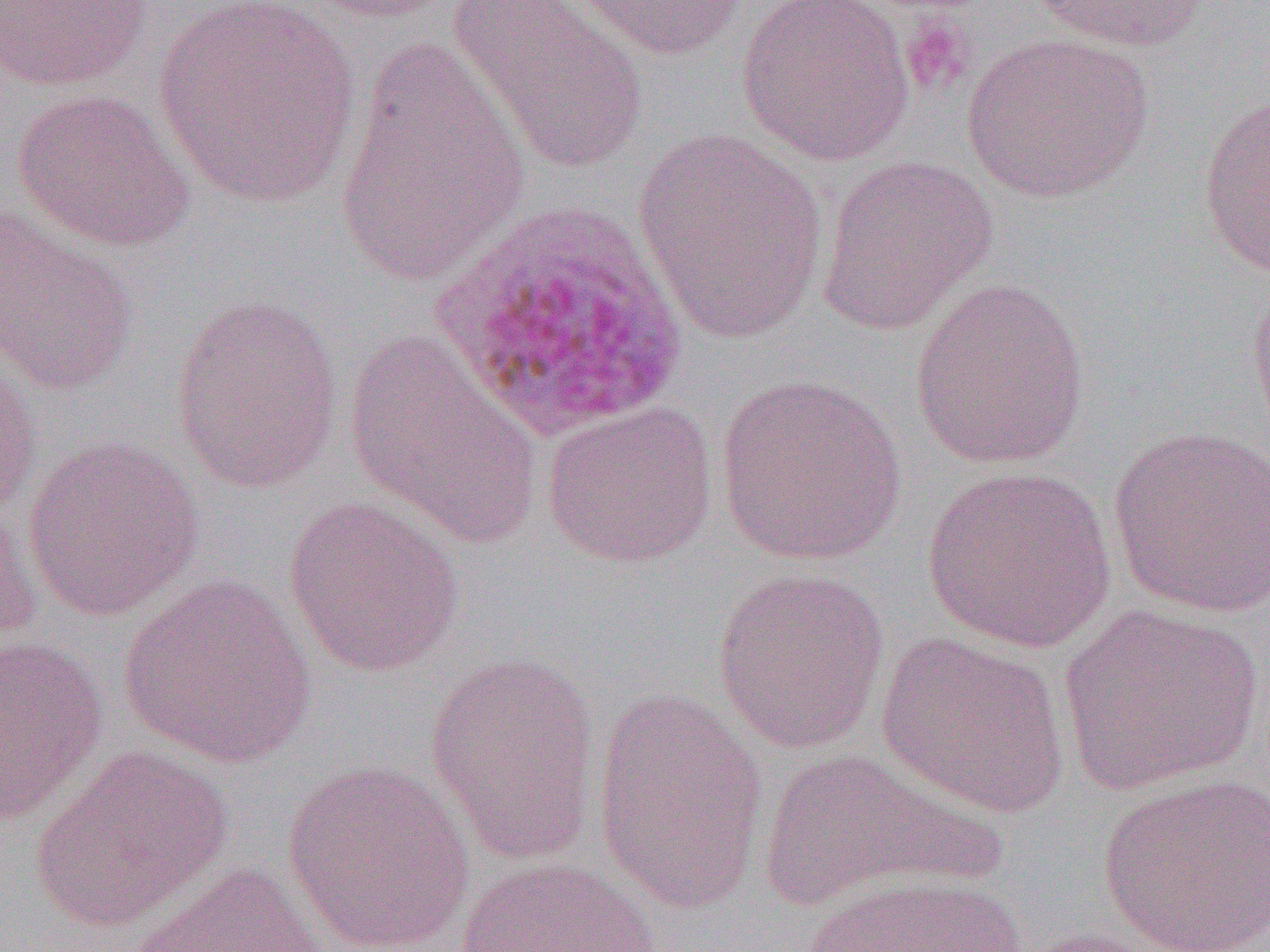
slide_level_diagnosis: Plasmodium ovale
magnification: 1000x
preparation: thin blood smear
platelet_locations: 'approximate bounding boxes as named x1/y1/x2/y2 corners in pixels: (x1=900, y1=14, x2=977, y2=94)'
uninfected_red_blood_cell_locations: 'approximate bounding boxes as named x1/y1/x2/y2 corners in pixels: (x1=1, y1=0, x2=153, y2=91), (x1=294, y1=0, x2=456, y2=23), (x1=447, y1=0, x2=650, y2=176), (x1=565, y1=0, x2=746, y2=62), (x1=735, y1=0, x2=919, y2=167), (x1=1030, y1=0, x2=1218, y2=53), (x1=151, y1=1, x2=365, y2=209), (x1=960, y1=32, x2=1155, y2=204), (x1=336, y1=34, x2=532, y2=291), (x1=11, y1=88, x2=194, y2=252), (x1=1198, y1=94, x2=1270, y2=279), (x1=632, y1=128, x2=831, y2=346), (x1=815, y1=154, x2=998, y2=335), (x1=0, y1=206, x2=141, y2=396), (x1=1247, y1=268, x2=1270, y2=450), (x1=909, y1=277, x2=1091, y2=469), (x1=169, y1=293, x2=343, y2=494), (x1=343, y1=329, x2=545, y2=552), (x1=0, y1=354, x2=42, y2=521), (x1=714, y1=372, x2=909, y2=566), (x1=540, y1=400, x2=718, y2=569), (x1=1106, y1=424, x2=1270, y2=619), (x1=21, y1=436, x2=205, y2=622), (x1=921, y1=465, x2=1117, y2=654), (x1=284, y1=496, x2=465, y2=677), (x1=0, y1=499, x2=41, y2=653), (x1=712, y1=566, x2=891, y2=754), (x1=117, y1=574, x2=318, y2=769), (x1=1057, y1=603, x2=1265, y2=795), (x1=875, y1=630, x2=1072, y2=820), (x1=1, y1=636, x2=109, y2=828), (x1=424, y1=652, x2=602, y2=865), (x1=590, y1=691, x2=769, y2=913), (x1=29, y1=746, x2=233, y2=932), (x1=757, y1=746, x2=998, y2=909), (x1=281, y1=759, x2=476, y2=952), (x1=1098, y1=773, x2=1270, y2=952), (x1=454, y1=857, x2=664, y2=952), (x1=129, y1=861, x2=337, y2=952), (x1=797, y1=873, x2=1032, y2=952), (x1=1008, y1=926, x2=1180, y2=952)'
plasmodium_ovale_infected_red_blood_cell_locations: 'approximate bounding boxes as named x1/y1/x2/y2 corners in pixels: (x1=427, y1=199, x2=692, y2=441)'
image_size: 1270×952 pixels
modality: light microscopy
field_of_view: single